Outline each blood parasite and name the species.
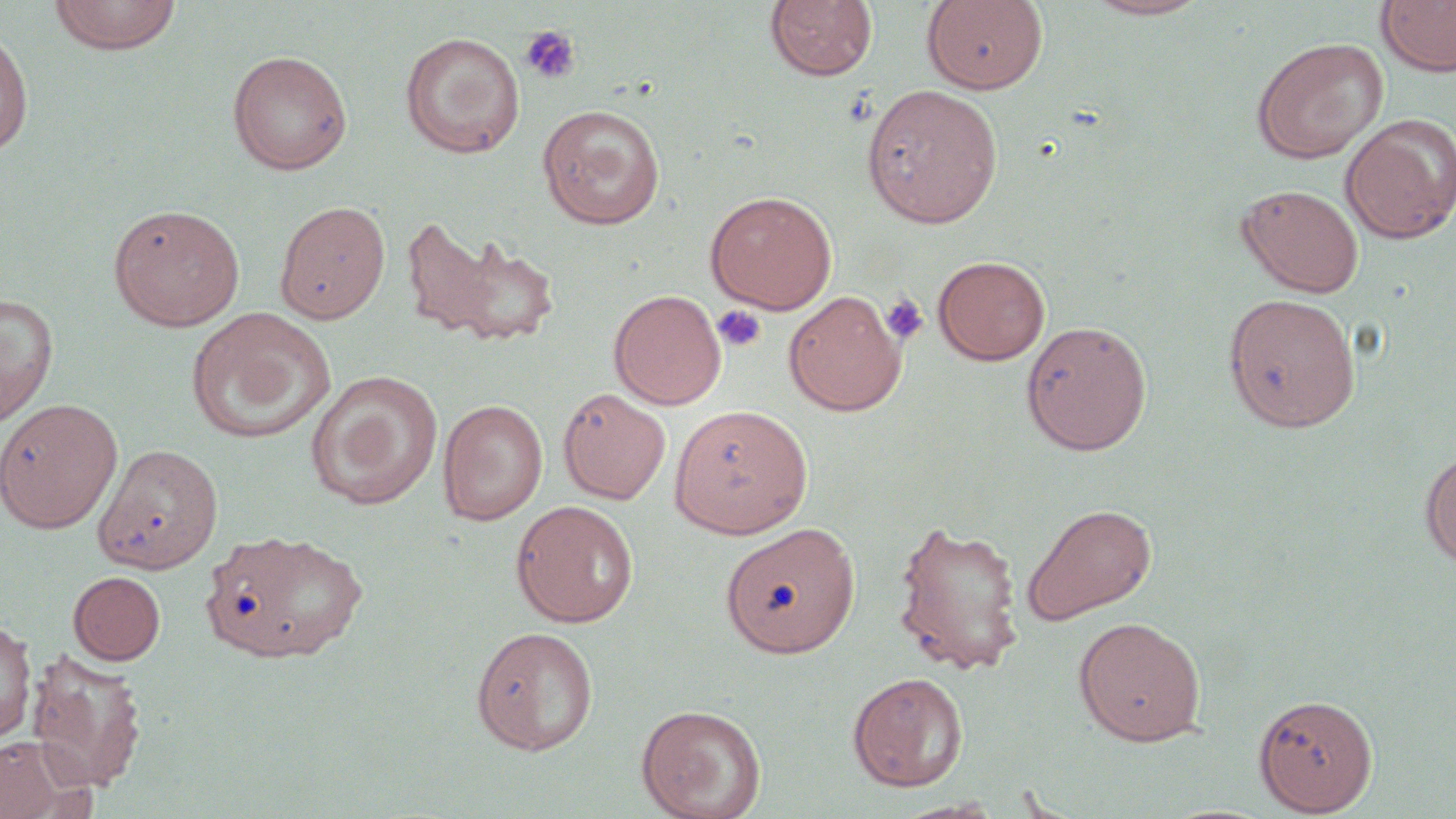
No blood parasites seen.

Approximate bounding boxes as named x1/y1/x2/y2 corners in pixels. Uninfected red blood cell locations: (x1=49, y1=0, x2=183, y2=55), (x1=923, y1=0, x2=1048, y2=95), (x1=1081, y1=0, x2=1215, y2=21), (x1=1376, y1=0, x2=1456, y2=77), (x1=764, y1=1, x2=877, y2=83), (x1=1, y1=22, x2=34, y2=161), (x1=400, y1=32, x2=525, y2=158), (x1=1251, y1=37, x2=1388, y2=163), (x1=226, y1=49, x2=353, y2=175), (x1=862, y1=83, x2=1004, y2=228), (x1=537, y1=104, x2=666, y2=229), (x1=1340, y1=114, x2=1456, y2=243), (x1=1236, y1=183, x2=1365, y2=297), (x1=704, y1=190, x2=837, y2=312), (x1=274, y1=201, x2=391, y2=323), (x1=108, y1=203, x2=245, y2=331), (x1=402, y1=219, x2=559, y2=348), (x1=933, y1=255, x2=1051, y2=365), (x1=609, y1=289, x2=727, y2=409), (x1=784, y1=290, x2=906, y2=416), (x1=0, y1=292, x2=59, y2=425), (x1=1223, y1=292, x2=1361, y2=432), (x1=186, y1=306, x2=336, y2=445), (x1=1020, y1=319, x2=1152, y2=455), (x1=306, y1=370, x2=443, y2=510), (x1=558, y1=387, x2=671, y2=505), (x1=0, y1=398, x2=123, y2=533), (x1=437, y1=399, x2=548, y2=525), (x1=669, y1=405, x2=813, y2=538), (x1=95, y1=442, x2=224, y2=574), (x1=1420, y1=452, x2=1456, y2=569), (x1=510, y1=500, x2=639, y2=628), (x1=1020, y1=501, x2=1157, y2=625), (x1=892, y1=517, x2=1026, y2=675), (x1=719, y1=522, x2=861, y2=657), (x1=201, y1=527, x2=369, y2=664), (x1=68, y1=571, x2=166, y2=665), (x1=1073, y1=616, x2=1207, y2=746), (x1=0, y1=621, x2=36, y2=743), (x1=470, y1=626, x2=599, y2=755), (x1=27, y1=650, x2=147, y2=792), (x1=847, y1=671, x2=968, y2=792), (x1=1253, y1=694, x2=1378, y2=815), (x1=5, y1=697, x2=130, y2=815), (x1=635, y1=703, x2=767, y2=819), (x1=0, y1=734, x2=90, y2=819), (x1=888, y1=798, x2=1008, y2=819). Platelet locations: (x1=520, y1=25, x2=582, y2=84), (x1=881, y1=293, x2=929, y2=345), (x1=711, y1=304, x2=767, y2=353). Slide-level diagnosis: negative for blood parasites. Single field of view. Light microscopy. May-Grünwald-Giemsa-stained preparation. Image is 1456×819 pixels. Thin blood smear. 1000x magnification.